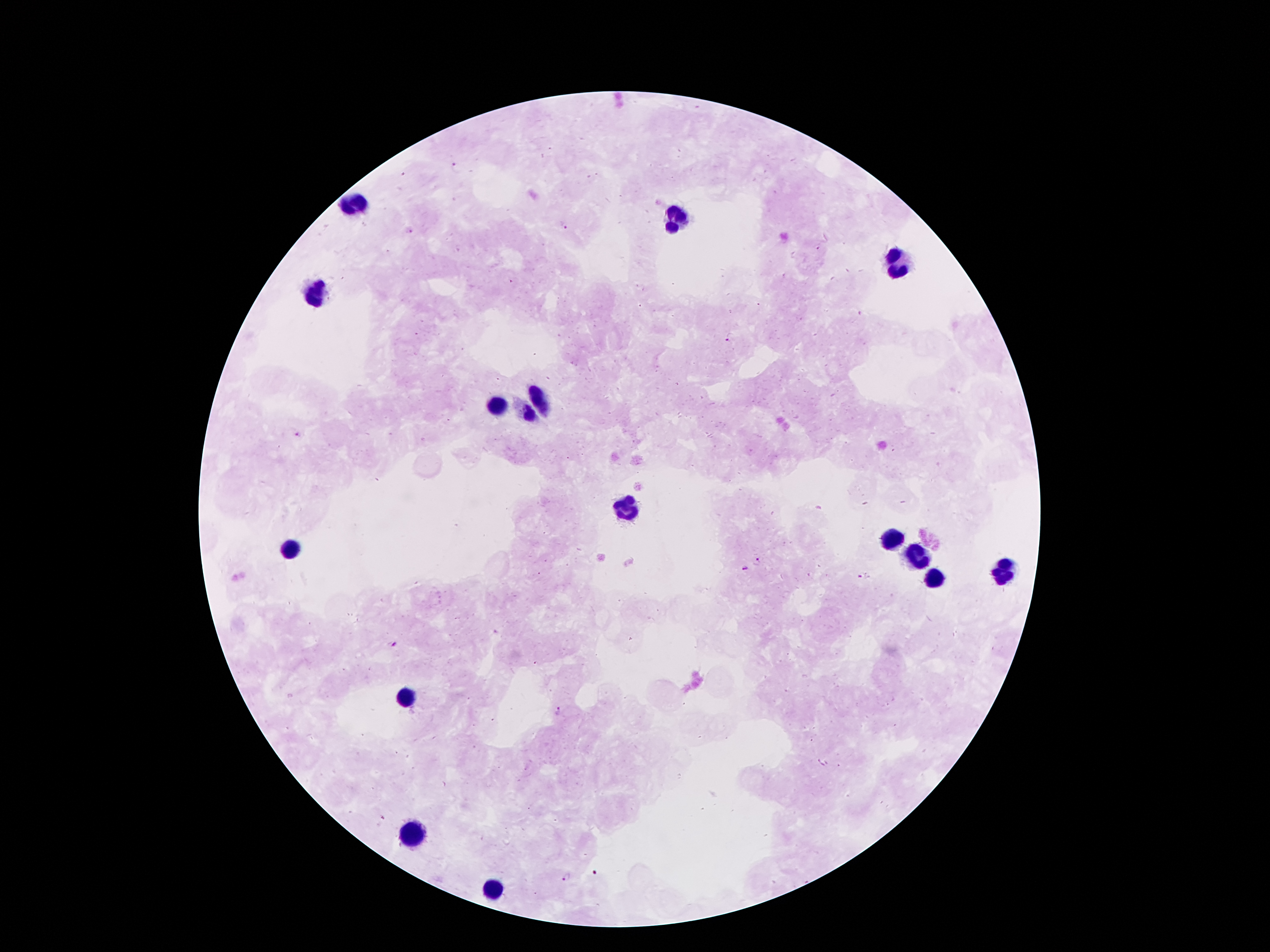 Approximate centers as {x, y} in pixels. Malaria parasite locations: {456, 166}, {403, 175}, {564, 226}, {409, 230}, {511, 282}, {730, 340}, {297, 433}, {759, 560}, {743, 570}, {863, 578}, {394, 645}, {559, 710}, {594, 872}, {564, 876}. Leukocyte locations: {353, 201}, {677, 220}, {895, 264}, {318, 294}, {540, 401}, {494, 407}, {528, 416}, {624, 508}, {891, 539}, {288, 546}, {914, 556}, {998, 573}, {931, 577}, {406, 697}, {414, 835}, {496, 890}. Single field of view. 100x magnification. Patient malaria status: infected with Plasmodium falciparum. Giemsa stain. Smartphone photograph taken through the microscope eyepiece. Thick blood smear. Image is 1270×952 pixels.